Describe the morphology of the erythrocytes.
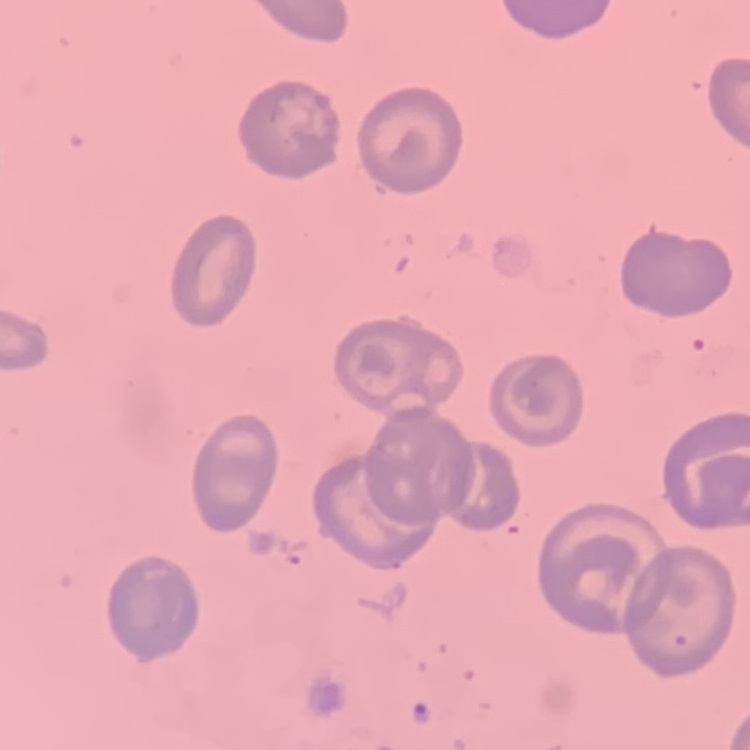
No rouleaux formation.

Summary:
  - Image type: one tile cut from a larger photomicrograph
  - Preparation: thin blood smear
  - Stain: Field's or Giemsa